Classify this cell by malaria status.
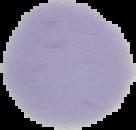

It is uninfected.

Image is 136×130 pixels. Cell region segmented out of the field of view; the surrounding area is masked to black. From a thin blood smear.